Report the malaria status of this cell.
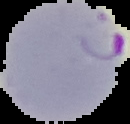

Parasitized.

{
  "preparation": "thin blood smear",
  "image_size": "130×124 pixels",
  "image_type": "segmented cell region on a black background"
}